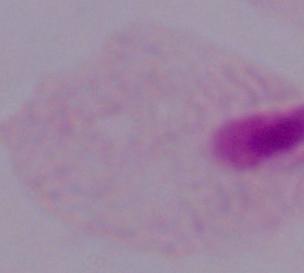
{
  "modality": "photomicrograph",
  "identification": "trichomonad",
  "magnification": "1000x"
}